Locate every malaria parasite.
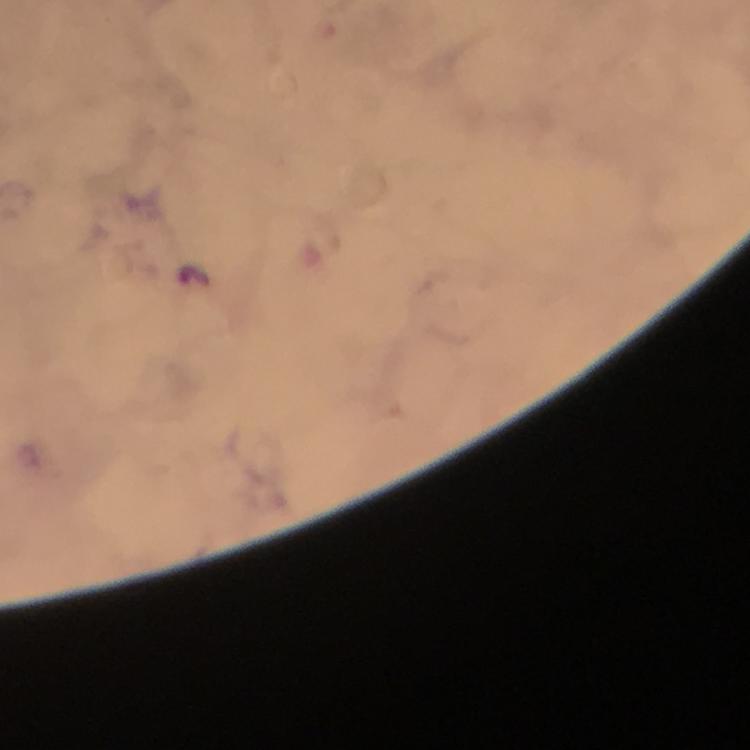
Approximate centers as (x, y) in pixels.
Malaria parasites: (196, 276).

Image is 750×750 pixels. 100x magnification. From a diagnostic examination for malaria. Immersion oil applied. Thick smear. Giemsa-stained preparation. Cropped region of a single field of view. Photographed with a smartphone mounted on the microscope.